Report the malaria status of this cell.
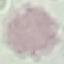

Uninfected.

Automatically extracted cell patch, resized to 64 × 64 pixels. Giemsa-stained preparation. Photographed with a smartphone camera at the microscope eyepiece. Thin blood smear.